Point out each leukocyte.
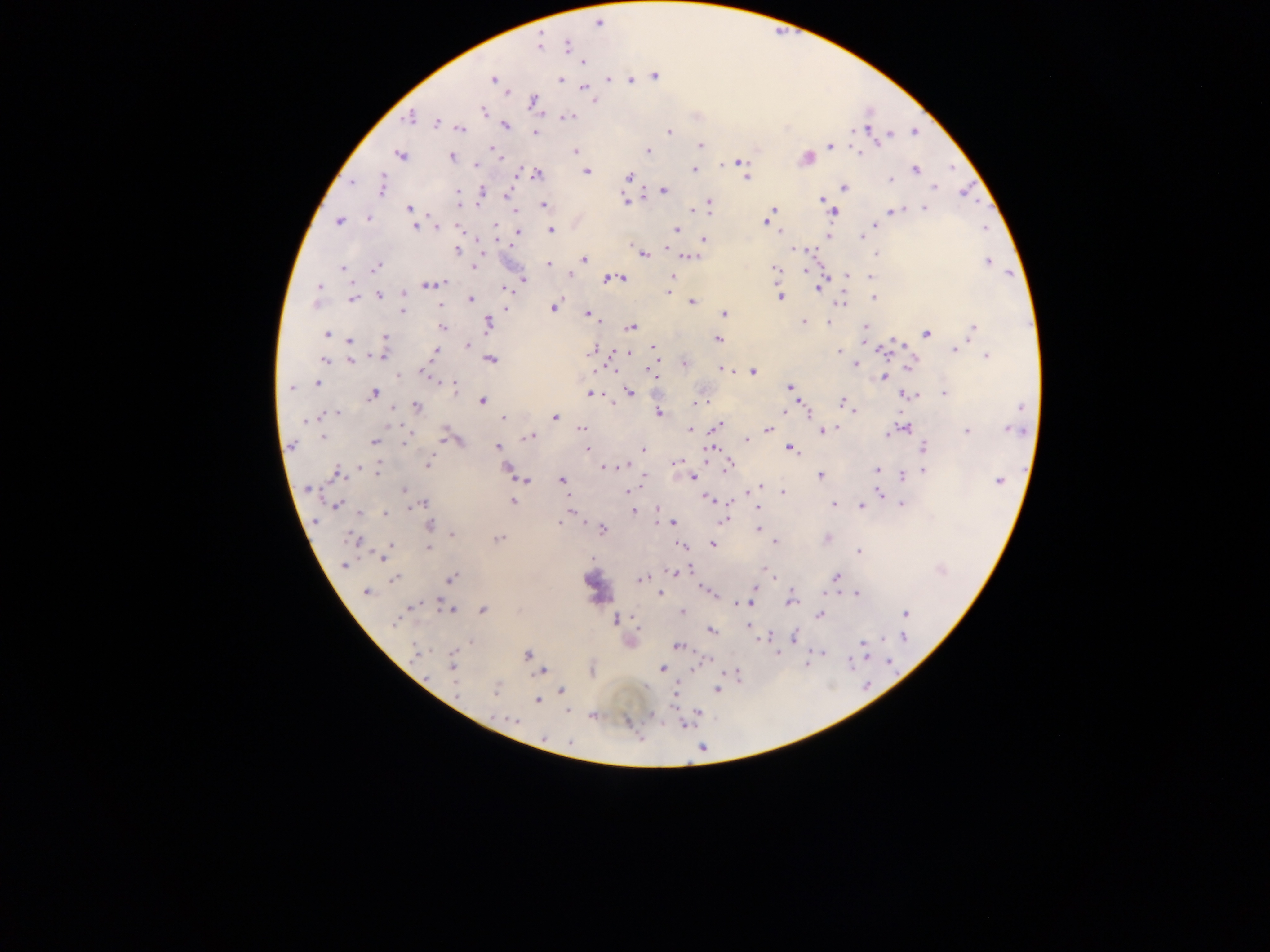
Approximate centers as x y in pixels.
Leukocytes: 596 584.

Summary:
  - Malaria parasite locations: 599 24; 539 45; 567 46; 583 62; 655 77; 609 79; 493 80; 560 80; 631 80; 585 89; 533 102; 483 111; 409 117; 570 117; 436 123; 506 125; 867 128; 461 129; 916 131; 669 132; 535 133; 890 135; 880 142; 700 145; 830 145; 493 149; 648 150; 575 151; 860 154; 400 155; 451 156; 806 158; 740 161; 475 165; 916 169; 694 170; 587 171; 538 174; 516 175; 629 175; 746 178; 890 180; 352 182; 382 185; 934 187; 845 188; 664 190; 458 191; 481 191; 506 194; 624 199; 821 200; 709 203; 826 204; 544 205; 408 208; 772 209; 924 209; 895 210; 691 211; 709 211; 832 213; 368 219; 338 221; 766 221; 495 225; 874 225; 416 227; 436 227; 457 227; 985 229; 550 230; 676 230; 518 231; 780 231; 861 236; 829 237; 704 239; 794 248; 456 250; 643 254; 876 255; 691 257; 585 260; 988 262; 548 263; 474 266; 375 267; 342 268; 775 269; 805 271; 570 275; 847 275; 672 277; 870 277; 620 278; 523 279; 607 279; 441 284; 433 285; 318 287; 818 287; 504 290; 668 291; 403 295; 380 296; 780 298; 874 298; 352 299; 471 300; 692 302; 842 303; 441 305; 553 308; 506 309; 402 311; 588 314; 724 314; 804 322; 828 322; 488 325; 442 327; 631 327; 865 327; 973 327; 327 334; 926 334; 384 337; 718 339; 350 340; 384 347; 467 347; 653 347; 593 349; 956 350; 839 351; 882 351; 435 352; 627 353; 381 355; 987 356; 324 359; 490 360; 351 361; 684 363; 855 364; 912 364; 722 369; 614 370; 595 371; 752 371; 422 372; 650 373; 399 376; 884 377; 317 383; 453 384; 290 387; 790 387; 629 391; 374 393; 591 394; 944 394; 908 395; 482 400; 697 403; 843 403; 418 406; 853 409; 783 412; 337 413; 659 413; 807 413; 327 414; 555 417; 503 418; 304 422; 717 426; 582 428; 835 428; 901 428; 690 429; 768 429; 1009 429; 967 430; 823 431; 889 433; 323 436; 530 436; 408 437; 445 437; 747 440; 374 442; 406 442; 292 444; 497 446; 923 447; 642 449; 711 449; 586 450; 791 450; 676 461; 427 465; 622 466; 729 466; 378 467; 605 467; 362 468; 507 468; 876 470; 925 470; 337 473; 820 476; 903 476; 692 477; 562 480; 999 480; 526 481; 759 487; 309 489; 404 491; 629 491; 783 492; 880 493; 708 499; 513 501; 424 504; 834 504; 902 504; 336 506; 862 506; 657 509; 633 511; 361 512; 385 513; 724 521; 560 522; 671 523; 431 526; 757 528; 602 529; 453 535; 353 539; 498 539; 828 539; 776 542; 712 544; 391 545; 682 546; 428 548; 859 551; 383 556; 344 565; 682 570; 766 571; 675 572; 837 577; 394 579; 451 579; 641 579; 755 588; 707 590; 366 592; 824 592; 660 594; 856 594; 790 602; 743 603; 412 606; 449 609; 483 609; 682 611; 906 613; 819 616; 616 619; 394 622; 749 626; 712 631; 767 637; 794 637; 904 638; 862 644; 677 647; 415 652; 818 652; 454 654; 527 654; 850 662; 889 663; 452 666; 662 668; 540 672; 737 672; 496 689; 562 690; 716 690; 456 691; 537 701; 593 716; 514 720; 542 737; 570 741
  - Preparation: thick blood smear
  - Country: Ghana
  - Capture: mobile-phone photograph through a microscope
  - Field of view: single
  - Image size: 1270×952 pixels